Classify this cell by malaria status.
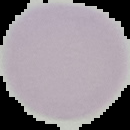

It is uninfected.

Summary:
  - Image size: 130×130 pixels
  - Image type: segmented cell region on a black background
  - Preparation: thin blood film